Name the blood parasite species.
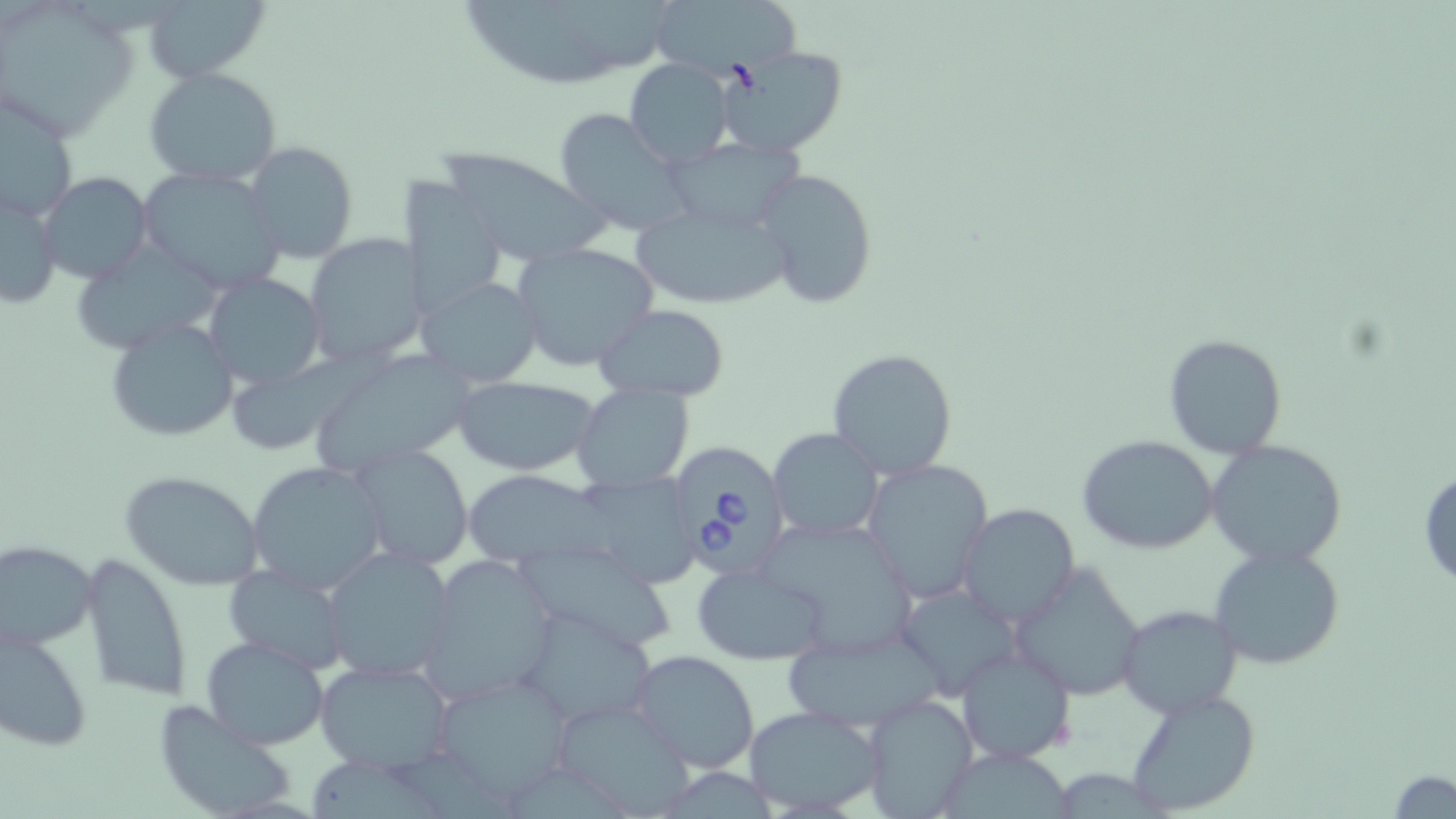
Babesia divergens.

field of view = one of a larger specimen
magnification = 1000x
preparation = thin blood film
Babesia divergens-infected red blood cell locations = approximate bounding boxes as [x1, y1, x2, y2] in pixels: [660, 439, 795, 586]
stain = May-Grünwald-Giemsa
uninfected red blood cell locations = approximate bounding boxes as [x1, y1, x2, y2] in pixels: [451, 0, 678, 89], [646, 0, 802, 81], [144, 1, 269, 82], [1, 3, 139, 139], [718, 46, 848, 160], [624, 60, 736, 169], [143, 67, 282, 187], [1, 100, 78, 224], [552, 108, 694, 239], [665, 137, 804, 233], [244, 141, 358, 263], [432, 147, 605, 267], [136, 165, 287, 294], [754, 168, 880, 309], [38, 171, 153, 286], [399, 182, 509, 313], [1, 183, 64, 311], [630, 201, 798, 309], [303, 233, 427, 367], [513, 241, 658, 372], [204, 272, 324, 387], [418, 275, 544, 388], [595, 305, 733, 399], [104, 317, 238, 443], [1161, 333, 1288, 458], [826, 347, 959, 481], [305, 355, 477, 479], [453, 375, 600, 477], [572, 384, 693, 491], [767, 428, 885, 542], [1077, 436, 1221, 555], [1205, 439, 1349, 567], [350, 444, 474, 570], [860, 458, 994, 605], [245, 460, 388, 596], [1417, 467, 1456, 590], [118, 468, 265, 591], [459, 472, 603, 564], [579, 472, 699, 587], [955, 504, 1080, 629], [748, 515, 919, 652], [518, 539, 676, 653], [0, 540, 97, 651], [1209, 544, 1346, 671], [321, 546, 456, 682], [79, 553, 191, 701], [420, 555, 559, 704], [691, 562, 832, 665], [1010, 563, 1146, 703], [222, 564, 351, 673], [894, 582, 1023, 700], [1116, 605, 1244, 717], [519, 608, 658, 729], [1, 621, 94, 753], [777, 626, 949, 733], [200, 635, 329, 749], [954, 642, 1077, 767], [630, 650, 762, 773], [315, 659, 454, 775], [428, 668, 574, 806], [1122, 688, 1260, 816], [861, 692, 977, 819], [548, 694, 699, 817], [150, 698, 300, 819], [741, 705, 885, 816], [944, 749, 1075, 818], [311, 761, 452, 819], [1055, 765, 1163, 819], [1386, 769, 1455, 818]
image size = 1456×819 pixels
modality = optical microscopy